Identify the preparation type.
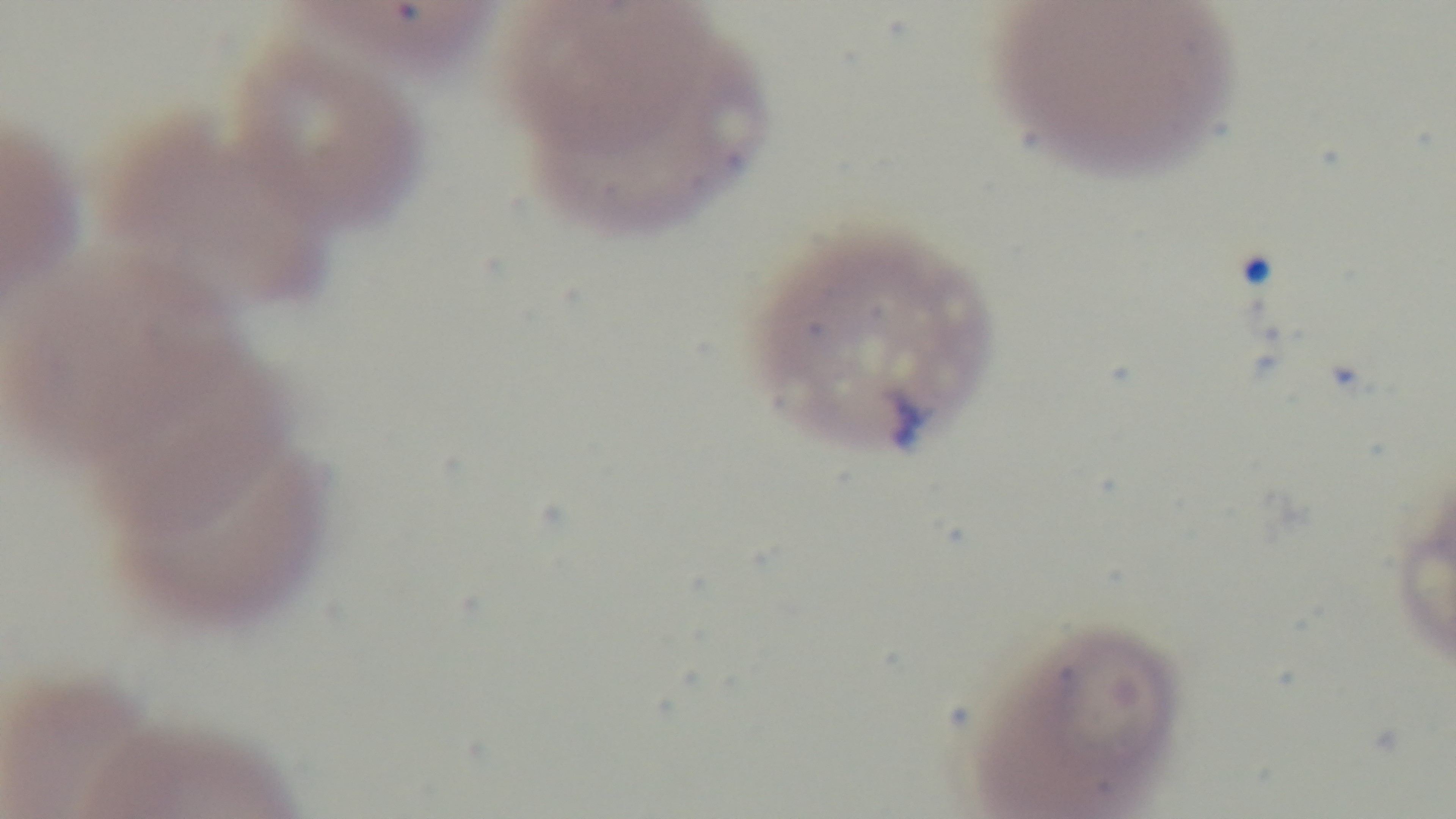

Thin.

field of view = one from the slide
modality = light microscopy
objective = 100x oil immersion
stain = Giemsa
capture = mounted 4K digital camera
malaria status = positive